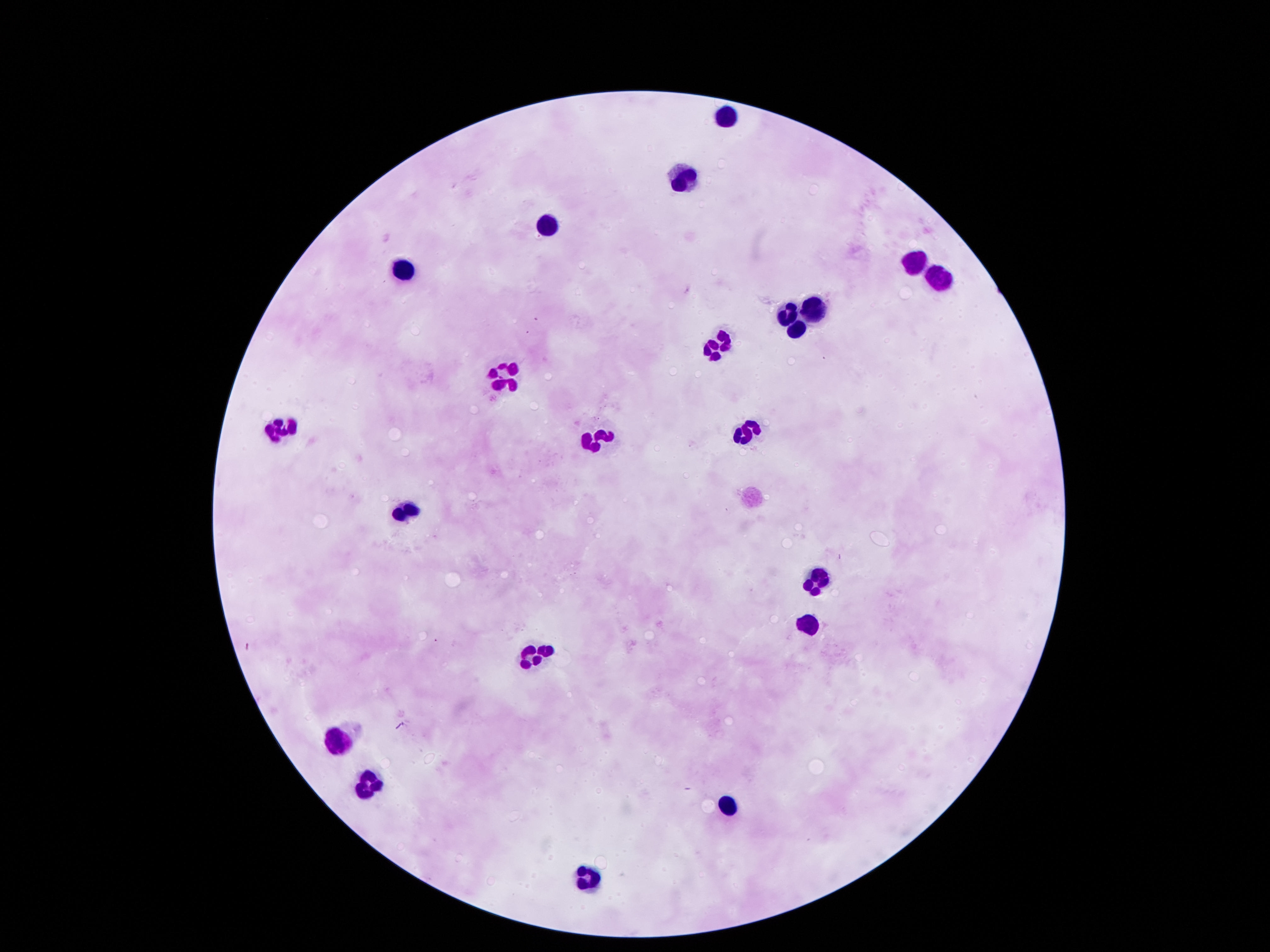

Approximate object centers, in pixels from the top-left corner. Leukocyte locations: (x=730, y=115), (x=684, y=176), (x=549, y=226), (x=913, y=260), (x=406, y=269), (x=937, y=278), (x=817, y=308), (x=790, y=313), (x=793, y=332), (x=722, y=343), (x=502, y=378), (x=283, y=429), (x=748, y=432), (x=594, y=440), (x=410, y=509), (x=815, y=577), (x=807, y=625), (x=534, y=656), (x=339, y=738), (x=368, y=784), (x=731, y=798), (x=590, y=880). Thick peripheral-blood smear. 100x magnification. Image is 1270×952 pixels. Giemsa stain. Photographed through the microscope eyepiece with a smartphone camera. One field from this slide. Patient malaria status: uninfected.